Classify this cell by malaria status.
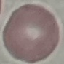

Uninfected.

Cell patch, automatically extracted from a larger field of view and resized to 64 × 64 pixels. Giemsa-stained preparation. Photographed with a smartphone camera at the microscope eyepiece. Thin blood smear.